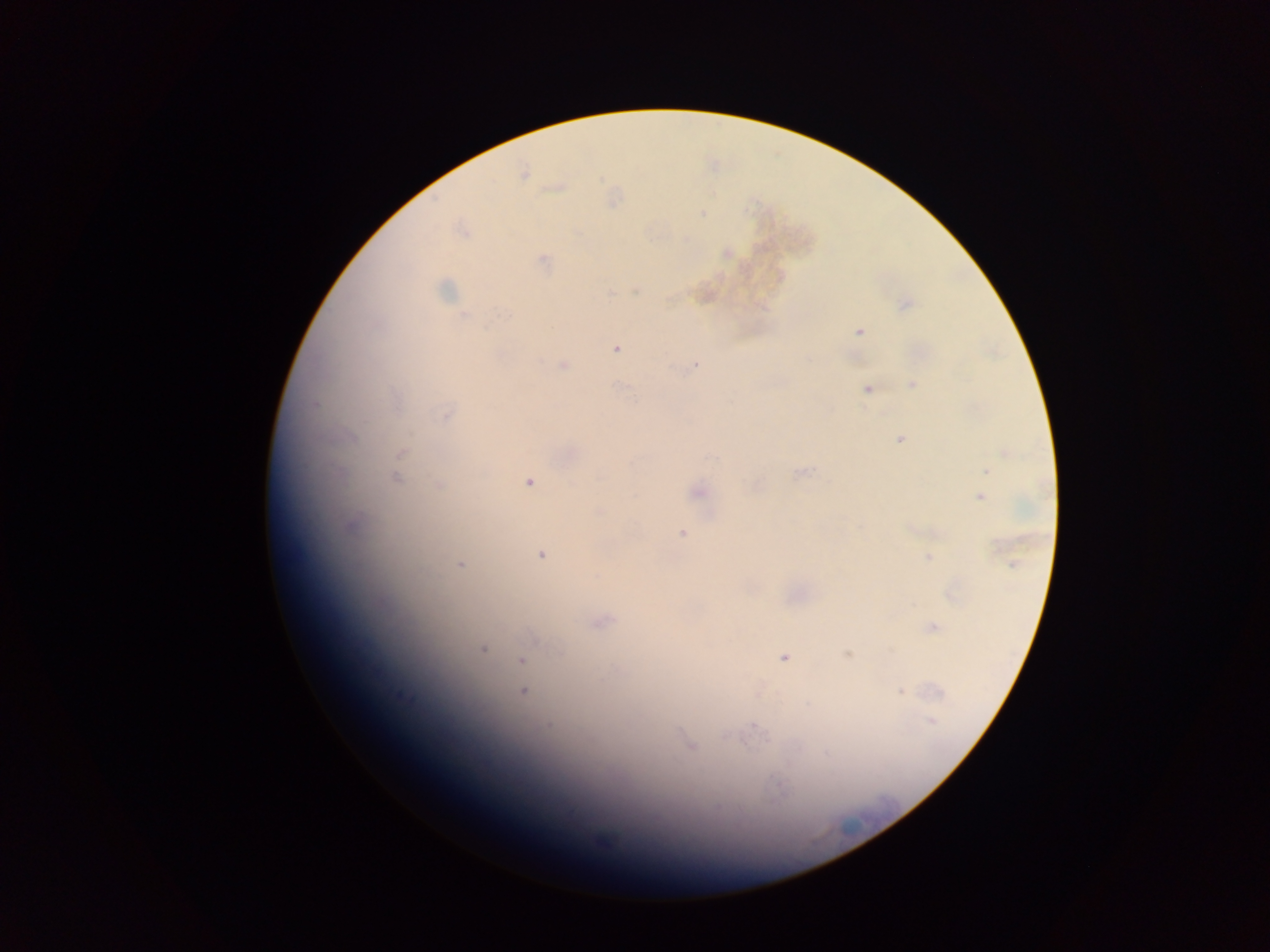

image size = 1270×952 pixels
malaria parasite locations = approximate centers as [x, y] in pixels: [523, 173], [556, 187], [702, 213], [461, 231], [725, 253], [542, 261], [635, 288], [445, 290], [905, 303], [859, 331], [615, 348], [696, 363], [563, 365], [912, 384], [867, 389], [446, 416], [899, 439], [401, 453], [568, 453], [1007, 453], [987, 471], [801, 472], [397, 477], [529, 481], [755, 484], [440, 486], [696, 491], [979, 496], [349, 525], [682, 533], [542, 555], [928, 557], [461, 564], [952, 593], [600, 621], [932, 627], [483, 648], [847, 654], [784, 657], [521, 660], [900, 691], [523, 692], [757, 692], [931, 721], [690, 746]
country = Ghana
preparation = thick blood film
field of view = single
capture = mobile-phone photograph through a microscope